Locate every malaria parasite and every leukocyte.
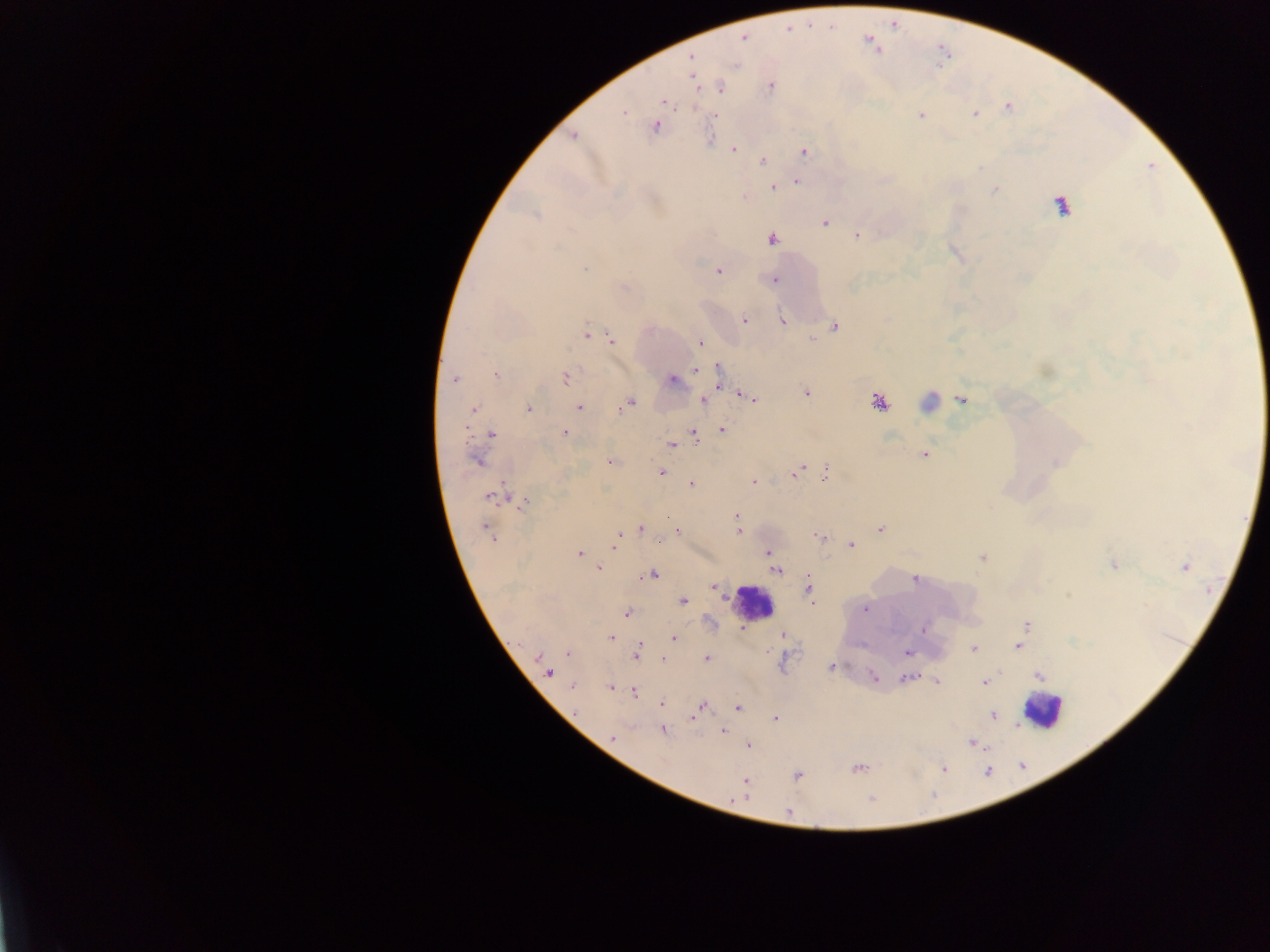

Approximate centers as {x, y} in pixels.
Malaria parasites: {743, 37}, {869, 40}, {691, 58}, {691, 68}, {693, 76}, {770, 86}, {720, 87}, {664, 102}, {1008, 106}, {623, 112}, {975, 114}, {713, 115}, {921, 115}, {655, 126}, {573, 135}, {710, 139}, {733, 149}, {804, 152}, {762, 160}, {799, 174}, {795, 180}, {772, 187}, {995, 189}, {744, 197}, {824, 222}, {857, 235}, {771, 238}, {585, 267}, {718, 271}, {774, 279}, {744, 319}, {782, 321}, {834, 326}, {585, 334}, {611, 338}, {813, 339}, {701, 343}, {719, 367}, {695, 369}, {495, 375}, {565, 377}, {454, 378}, {671, 380}, {718, 380}, {805, 392}, {742, 395}, {751, 398}, {962, 398}, {703, 400}, {877, 400}, {930, 402}, {627, 404}, {578, 406}, {527, 408}, {472, 409}, {722, 429}, {565, 433}, {693, 433}, {491, 434}, {671, 444}, {924, 454}, {477, 461}, {609, 461}, {798, 470}, {659, 471}, {826, 471}, {753, 482}, {691, 483}, {492, 497}, {523, 502}, {736, 516}, {640, 528}, {738, 528}, {880, 528}, {678, 530}, {488, 531}, {818, 537}, {617, 540}, {658, 541}, {852, 544}, {768, 551}, {579, 553}, {982, 558}, {772, 559}, {1113, 564}, {1184, 567}, {598, 568}, {777, 569}, {651, 574}, {915, 578}, {713, 586}, {808, 588}, {682, 600}, {864, 609}, {626, 613}, {1026, 625}, {742, 629}, {923, 629}, {782, 635}, {611, 637}, {674, 638}, {1018, 646}, {973, 648}, {636, 651}, {907, 651}, {568, 652}, {707, 658}, {663, 659}, {831, 667}, {548, 671}, {1002, 671}, {1038, 675}, {873, 677}, {906, 677}, {936, 680}, {985, 682}, {572, 685}, {611, 686}, {635, 692}, {662, 703}, {700, 705}, {737, 708}, {993, 715}, {775, 718}, {662, 730}, {724, 730}, {612, 737}, {972, 742}, {749, 745}, {856, 768}, {942, 768}, {797, 775}, {745, 781}, {788, 811}.
Leukocytes: {1060, 204}, {753, 602}, {1042, 709}.

Sample from Ghana. Image is 1270×952 pixels. One field of view. Thick blood film. Mobile-phone photograph taken through the microscope.